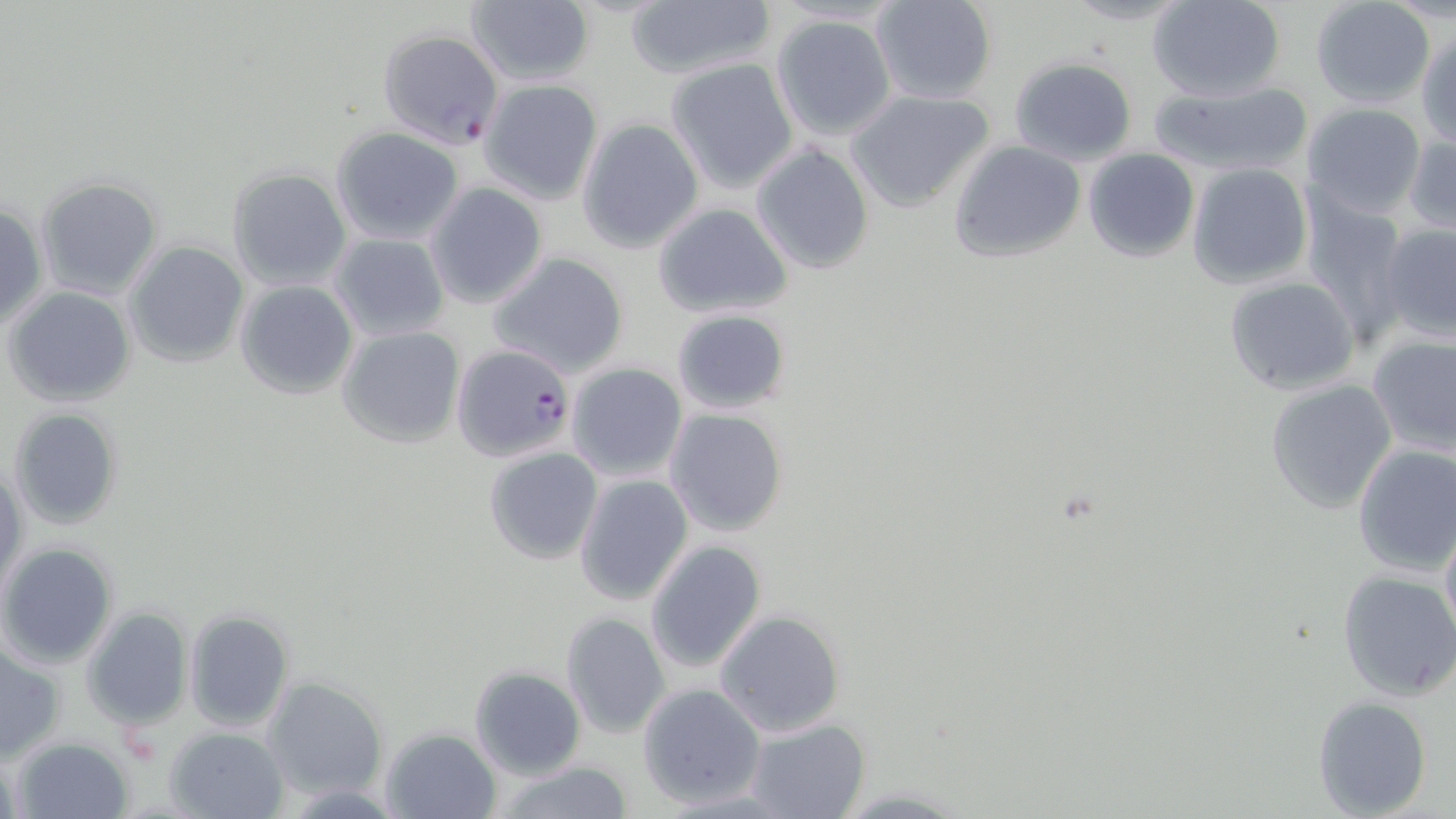
Summary:
  - Coordinate format: approximate bounding boxes as [x1, y1, x2, y2] in pixels
  - Uninfected red blood cell locations: [869, 0, 998, 105], [1057, 0, 1194, 25], [1148, 0, 1285, 102], [1309, 1, 1436, 108], [464, 2, 595, 87], [625, 2, 775, 80], [770, 13, 897, 141], [1418, 31, 1456, 148], [665, 57, 801, 193], [1008, 57, 1136, 165], [478, 78, 604, 205], [1150, 79, 1315, 176], [845, 89, 995, 214], [1302, 103, 1428, 219], [578, 117, 705, 253], [331, 126, 464, 245], [1405, 132, 1455, 237], [949, 140, 1086, 263], [750, 143, 876, 274], [1082, 147, 1199, 262], [1186, 162, 1313, 287], [226, 165, 351, 290], [35, 177, 162, 298], [424, 183, 548, 307], [1302, 196, 1408, 338], [650, 202, 794, 319], [0, 204, 48, 330], [1377, 221, 1456, 344], [329, 232, 449, 341], [123, 241, 250, 368], [486, 251, 630, 376], [1224, 274, 1361, 395], [234, 279, 358, 399], [6, 286, 134, 407], [671, 309, 792, 417], [336, 325, 466, 449], [1366, 333, 1456, 455], [566, 363, 688, 482], [1265, 379, 1397, 513], [7, 406, 123, 530], [664, 407, 788, 537], [1352, 443, 1456, 577], [483, 445, 603, 565], [0, 461, 27, 599], [573, 472, 695, 606], [1439, 517, 1456, 648], [645, 541, 767, 673], [0, 542, 119, 666], [1337, 569, 1456, 703], [82, 607, 193, 729], [183, 608, 294, 731], [715, 609, 845, 737], [560, 613, 671, 738], [1, 646, 64, 763], [470, 665, 586, 778], [261, 675, 390, 803], [637, 683, 764, 808], [1312, 696, 1432, 818], [742, 716, 872, 819], [165, 726, 290, 819], [381, 728, 502, 819], [11, 735, 136, 819], [492, 761, 639, 819]
  - Plasmodium falciparum-infected red blood cell locations: [376, 27, 503, 149], [458, 343, 571, 461]
  - Slide-level diagnosis: Plasmodium falciparum
  - Magnification: 1000x
  - Field of view: one of a larger specimen
  - Stain: May-Grünwald-Giemsa
  - Preparation: thin blood smear
  - Image size: 1456×819 pixels
  - Modality: optical microscopy